Locate platelets.
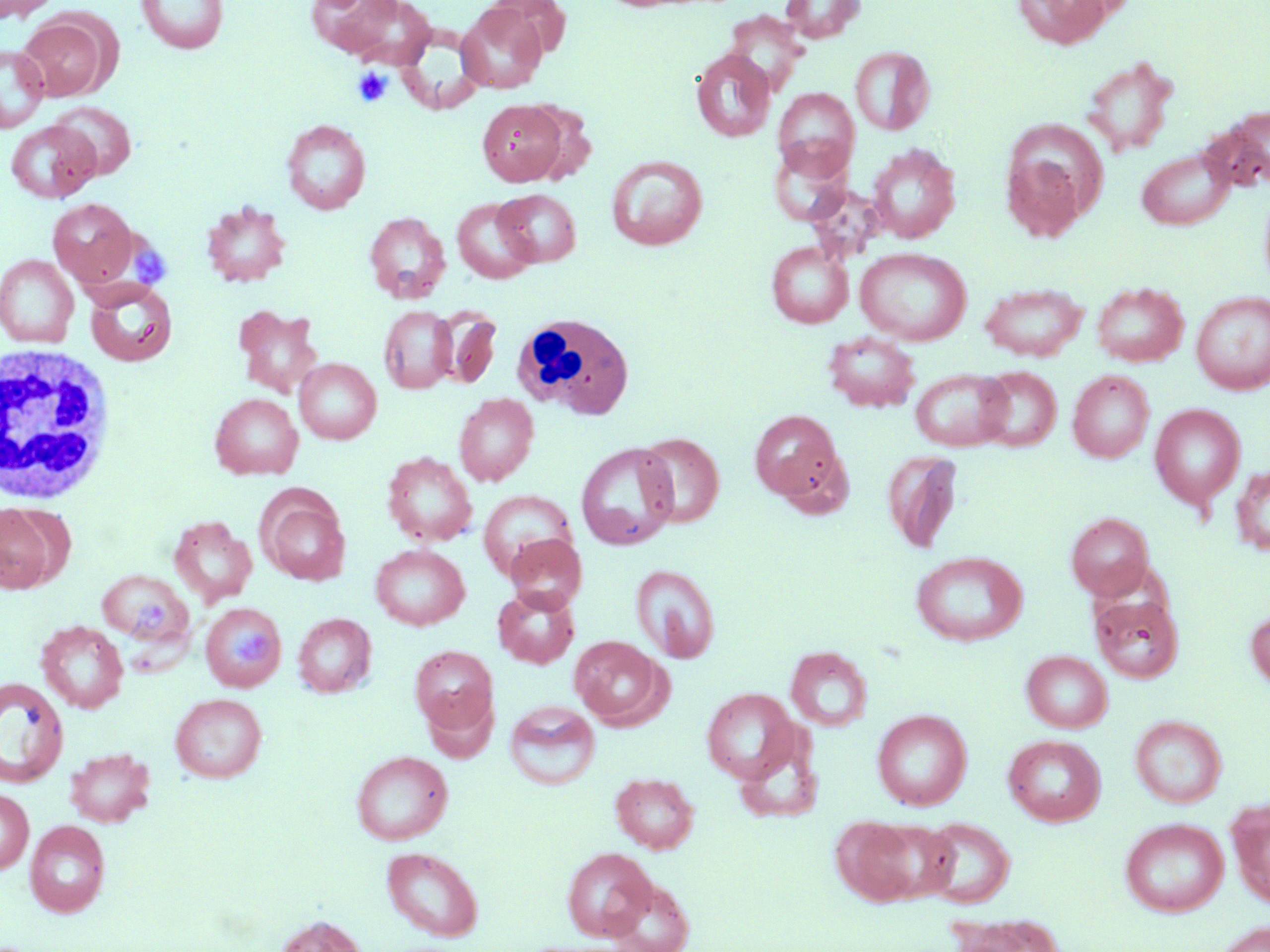

Approximate bounding boxes as [x1, y1, x2, y2] in pixels.
Platelets: [352, 67, 392, 107], [134, 247, 171, 287], [136, 593, 168, 636], [234, 631, 274, 665].

Uninfected red blood cell locations: [136, 0, 229, 54], [307, 0, 407, 58], [339, 0, 437, 69], [781, 0, 865, 43], [1013, 0, 1113, 49], [0, 1, 60, 21], [456, 4, 548, 94], [724, 10, 808, 93], [16, 16, 111, 101], [0, 44, 49, 132], [851, 46, 934, 136], [691, 48, 776, 142], [1081, 55, 1178, 156], [773, 88, 860, 177], [477, 99, 567, 186], [48, 101, 137, 179], [523, 103, 598, 184], [281, 119, 371, 214], [6, 120, 100, 203], [1005, 120, 1108, 218], [770, 142, 855, 228], [866, 144, 960, 243], [1136, 147, 1234, 230], [1002, 152, 1087, 242], [606, 155, 708, 250], [495, 189, 581, 267], [451, 197, 540, 284], [47, 198, 139, 287], [201, 201, 291, 287], [364, 212, 450, 303], [766, 242, 853, 328], [855, 247, 972, 345], [0, 254, 79, 348], [85, 281, 178, 367], [1091, 281, 1189, 367], [980, 283, 1088, 361], [1191, 291, 1270, 394], [232, 304, 324, 398], [378, 305, 458, 394], [430, 307, 502, 388], [823, 331, 919, 412], [295, 358, 381, 444], [976, 367, 1061, 451], [911, 368, 1013, 452], [1068, 370, 1155, 463], [210, 393, 303, 480], [454, 393, 539, 486], [1149, 404, 1245, 509], [749, 409, 848, 509], [635, 432, 724, 529], [576, 442, 679, 551], [881, 450, 962, 553], [382, 451, 478, 546], [1230, 464, 1270, 556], [258, 491, 351, 585], [478, 491, 576, 580], [1, 502, 66, 592], [1065, 512, 1154, 599], [168, 516, 257, 607], [504, 533, 587, 613], [370, 544, 470, 630], [910, 550, 1028, 647], [631, 564, 720, 663], [98, 569, 191, 647], [493, 586, 580, 668], [1091, 593, 1184, 684], [199, 602, 287, 692], [1246, 608, 1270, 691], [292, 613, 376, 697], [36, 620, 128, 713], [570, 636, 670, 728], [410, 645, 498, 735], [786, 646, 872, 731], [1021, 650, 1113, 733], [0, 677, 69, 787], [702, 688, 799, 783], [170, 693, 267, 783], [504, 700, 601, 791], [872, 709, 972, 811], [1130, 715, 1227, 808], [1003, 734, 1106, 826], [64, 747, 155, 827], [351, 750, 453, 845], [610, 771, 699, 853], [0, 788, 33, 874], [1228, 799, 1270, 909], [830, 815, 924, 906], [920, 817, 1015, 908], [1120, 817, 1228, 918], [866, 819, 957, 903], [24, 820, 111, 918], [382, 846, 484, 941], [562, 846, 657, 940], [602, 878, 695, 952], [948, 912, 1065, 952], [275, 915, 367, 952], [1213, 921, 1270, 952]. White blood cell locations: [512, 312, 634, 420], [2, 342, 117, 506]. Slide-level diagnosis: negative for blood parasites. Captured at 1000x magnification. May-Grünwald-Giemsa-stained preparation. Image is 1270×952 pixels. Thin blood smear. Light microscopy. One field of a larger specimen.